Describe the morphology of the erythrocytes.
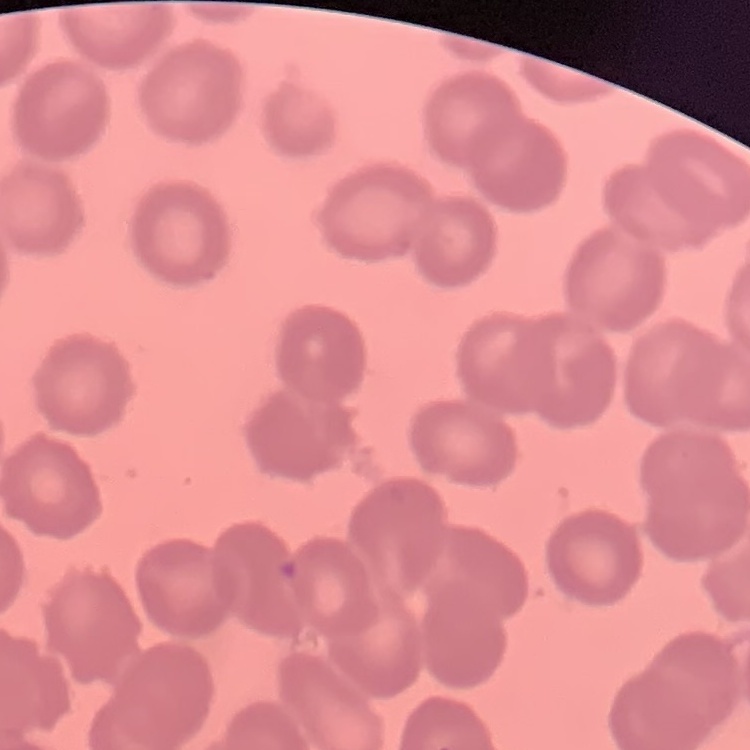

No rouleaux formation.

Field's or Giemsa stain. Thin blood film. One tile cut from a larger photomicrograph.